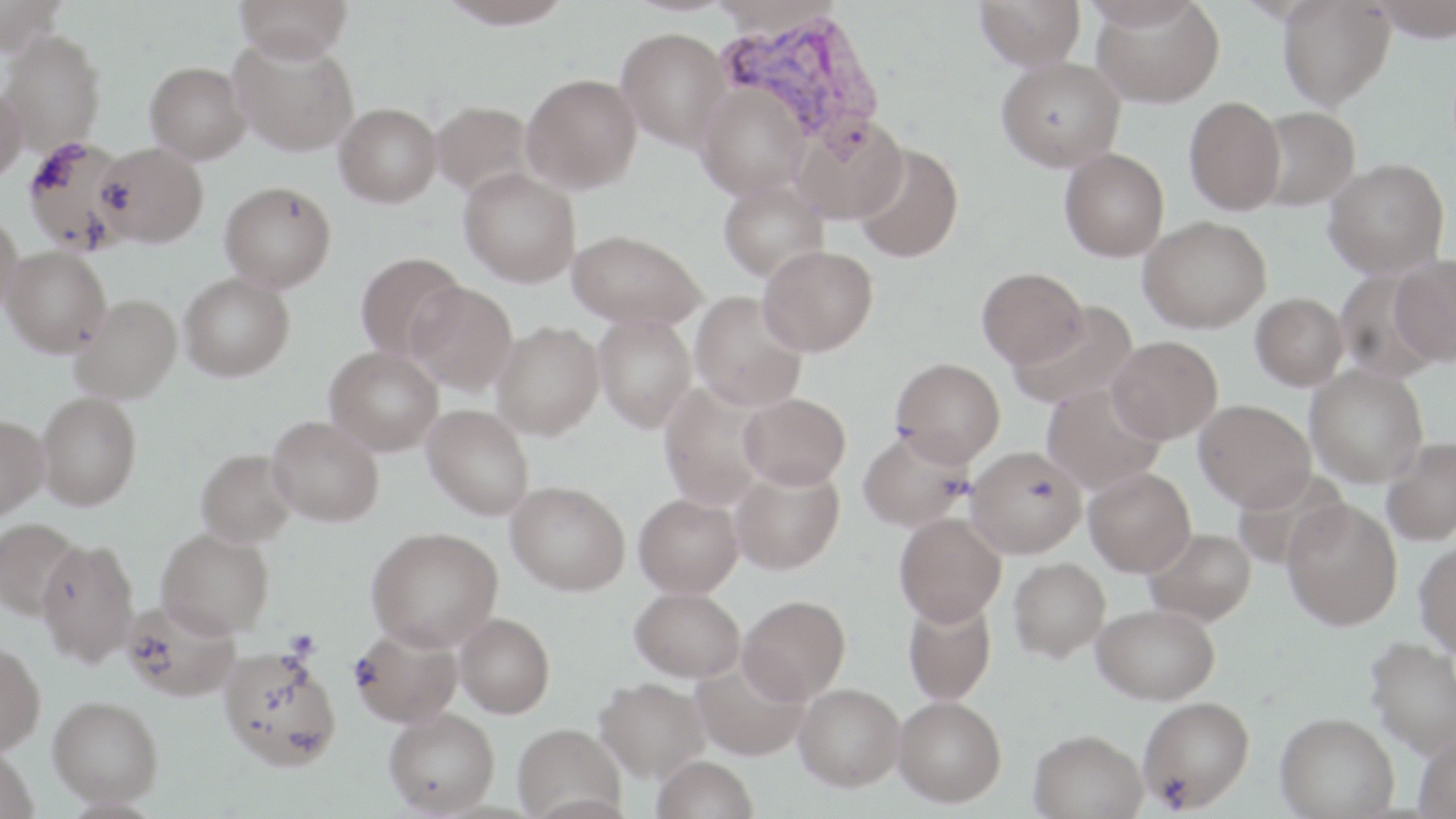 Approximate bounding boxes as (x1, y1, x2, y2) in pixels. Platelet locations: (284, 629, 320, 660). Uninfected red blood cell locations: (0, 0, 65, 58), (235, 0, 353, 64), (438, 0, 575, 29), (974, 0, 1086, 70), (1278, 0, 1395, 110), (1369, 0, 1456, 42), (1075, 1, 1206, 30), (1093, 1, 1224, 108), (616, 27, 733, 151), (0, 30, 105, 156), (229, 34, 359, 157), (996, 57, 1125, 171), (144, 61, 251, 164), (522, 73, 643, 193), (696, 82, 810, 200), (0, 83, 27, 185), (1184, 96, 1286, 215), (430, 100, 535, 199), (335, 103, 442, 207), (1254, 106, 1361, 211), (791, 115, 909, 225), (21, 136, 133, 255), (96, 142, 209, 248), (852, 142, 964, 262), (1060, 148, 1170, 261), (1324, 158, 1449, 278), (459, 168, 581, 287), (718, 178, 829, 283), (220, 181, 336, 292), (0, 210, 23, 318), (1139, 215, 1272, 333), (567, 229, 706, 330), (758, 245, 878, 356), (2, 246, 112, 357), (355, 252, 467, 362), (1389, 254, 1456, 366), (977, 267, 1088, 368), (1335, 268, 1440, 382), (179, 272, 294, 381), (406, 281, 518, 396), (690, 291, 807, 411), (1250, 292, 1348, 391), (71, 294, 182, 403), (1011, 301, 1138, 410), (594, 314, 696, 432), (491, 321, 604, 439), (1108, 336, 1222, 443), (324, 345, 444, 456), (891, 358, 1005, 468), (1305, 365, 1428, 487), (1042, 381, 1167, 494), (658, 382, 771, 511), (37, 391, 141, 510), (738, 392, 851, 490), (1194, 399, 1316, 512), (421, 404, 534, 520), (0, 414, 48, 520), (267, 415, 384, 527), (859, 429, 973, 532), (1381, 436, 1456, 545), (966, 445, 1088, 559), (195, 448, 298, 547), (728, 463, 845, 575), (1084, 467, 1196, 577), (506, 480, 630, 595), (634, 493, 744, 597), (1282, 498, 1403, 630), (893, 512, 1006, 627), (0, 518, 83, 621), (366, 526, 503, 651), (156, 527, 274, 638), (1145, 527, 1256, 625), (36, 538, 140, 666), (1414, 541, 1456, 657), (1009, 557, 1111, 662), (630, 587, 746, 682), (738, 595, 850, 703), (902, 595, 997, 705), (122, 599, 240, 702), (1092, 603, 1220, 705), (455, 613, 555, 718), (351, 626, 462, 728), (1365, 637, 1456, 758), (0, 641, 45, 755), (217, 646, 341, 771), (692, 658, 810, 762), (594, 677, 710, 782), (794, 684, 905, 791), (48, 695, 162, 805), (893, 695, 1006, 807), (1138, 696, 1255, 812), (384, 708, 499, 815), (1275, 712, 1399, 818), (513, 724, 625, 819), (1029, 729, 1147, 819), (1414, 730, 1456, 817), (0, 746, 38, 818), (652, 755, 758, 818). Plasmodium vivax-infected red blood cell locations: (717, 8, 887, 148). Slide-level diagnosis: Plasmodium vivax. 1000x magnification. Image is 1456×819 pixels. One field of a larger specimen. May-Grünwald-Giemsa stain. Thin blood smear. Light microscopy.